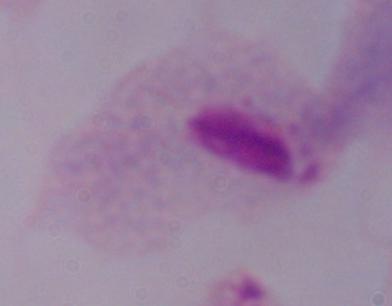
modality: micrograph
magnification: 1000x
identification: trichomonad